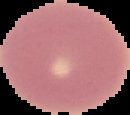

image size = 130×115 pixels
preparation = thin blood smear
image type = cell region segmented out of the field of view; surrounding area masked to black
result = negative for Plasmodium parasites